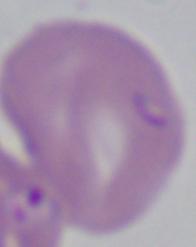
magnification = 1000x
modality = micrograph
identification = Babesia